Report the malaria status of this cell.
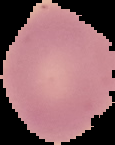
It is uninfected.

image type = segmented cell region with the area outside set to black
preparation = thin blood film
image size = 115×145 pixels